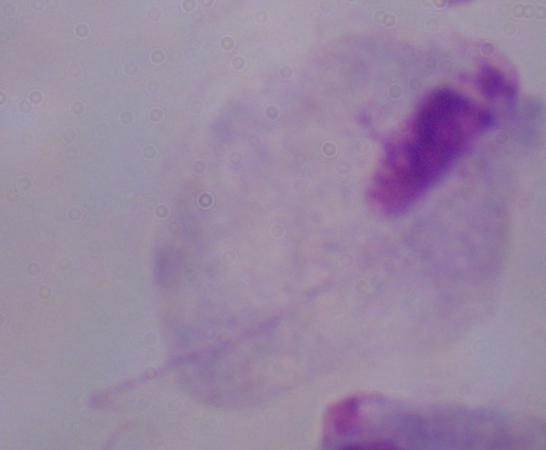
{
  "modality": "micrograph",
  "magnification": "1000x",
  "identification": "trichomonad"
}